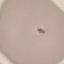
malaria_status: uninfected
capture: smartphone camera at the microscope eyepiece
stain: Giemsa
preparation: thin blood smear
image_type: automatically extracted cell patch, resized to 64 × 64 pixels